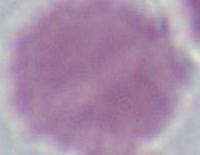

modality: micrograph
magnification: 1000x
identification: red blood cell